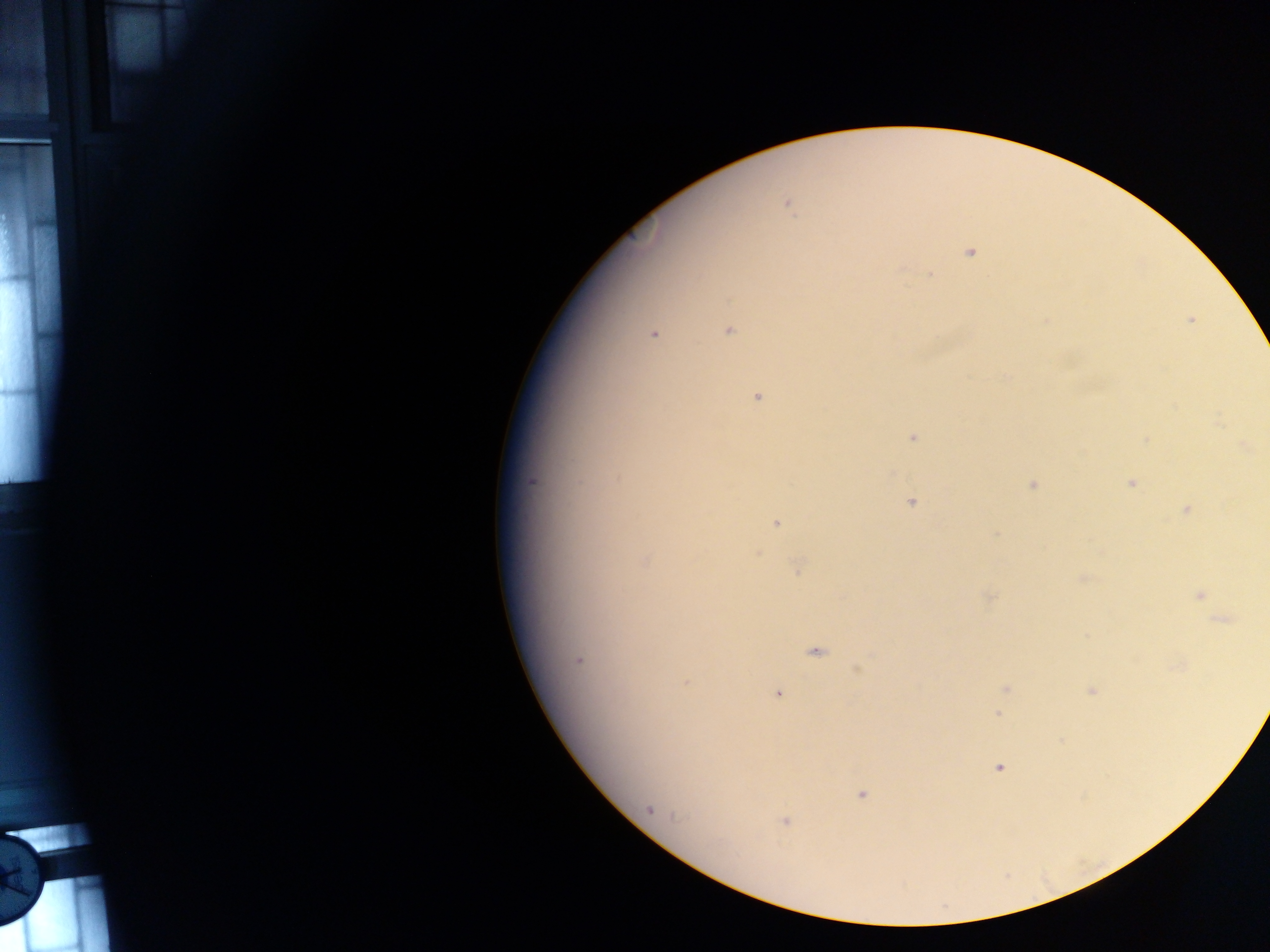 Approximate centers as (x, y) in pixels. Plasmodium parasite locations: (788, 205), (970, 253), (931, 275), (1191, 320), (729, 331), (652, 334), (757, 397), (912, 437), (1243, 446), (531, 481), (1130, 483), (1032, 485), (911, 501), (1186, 509), (776, 523), (996, 533), (758, 553), (646, 562), (798, 569), (1082, 579), (1200, 595), (989, 597), (1222, 620), (816, 653), (579, 660), (858, 669), (686, 683), (1005, 689), (1091, 690), (777, 693), (998, 714), (999, 768), (861, 795), (650, 809), (785, 821). Single field of view. Mobile-phone photograph taken through the microscope. Thick blood smear. Collected in Ghana. Image is 1270×952 pixels.